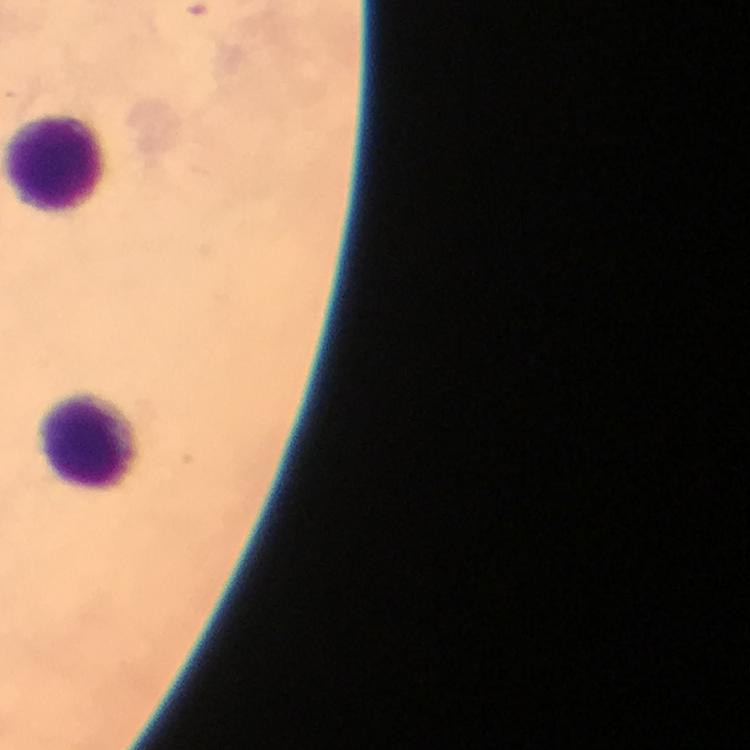
{
  "magnification": "100x",
  "malaria_parasites": "none detected",
  "image_size": "750×750 pixels",
  "leukocyte_locations": "approximate centers as [x, y] in pixels: [56, 163], [93, 443]",
  "preparation": "thick smear",
  "cropped_from": "a single field of view",
  "capture": "smartphone mounted on the microscope",
  "immersion_oil": "applied",
  "stain": "Giemsa",
  "context": "from a diagnostic examination for malaria"
}